Report the malaria status of this cell.
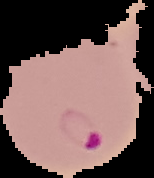

It is parasitized.

The area outside the segmented cell region is set to black. From a thin blood smear. Image is 154×178 pixels.